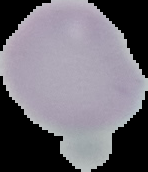

From a thin blood film. Result: negative for Plasmodium parasites. Image is 148×172 pixels. Segmented cell region on a black background.